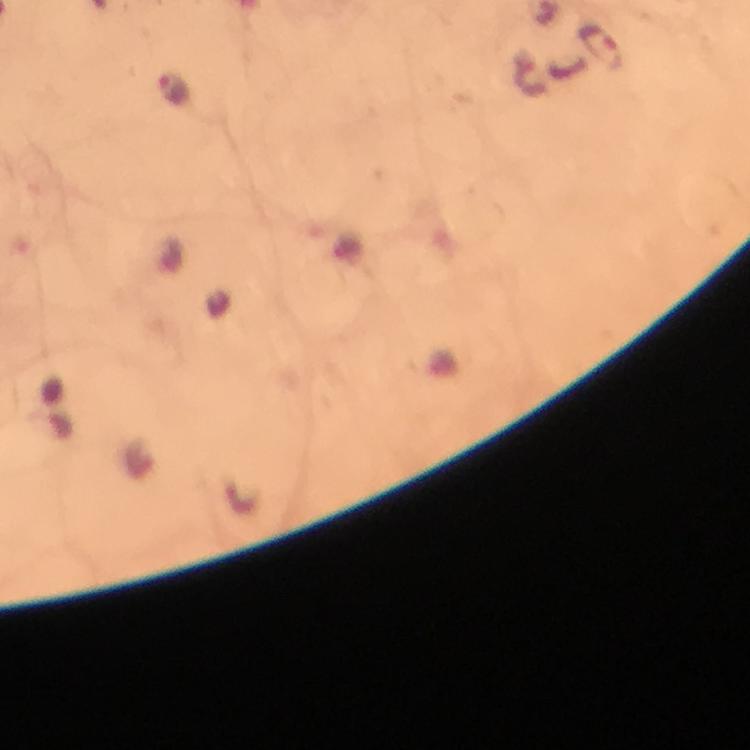 Approximate object centers, in pixels from the top-left corner. Malaria parasite locations: (x=601, y=48), (x=175, y=88). Image is 750×750 pixels. Thick blood film. Giemsa stain. From a diagnostic examination for malaria. A crop from one field of view. Smartphone photograph taken through a microscope. At 100x magnification. Immersion oil was used.